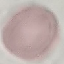
malaria_status: uninfected
capture: smartphone through the microscope eyepiece
image_type: cell patch, automatically extracted from a larger field of view and resized to 64 × 64 pixels
preparation: thin blood smear
stain: Giemsa